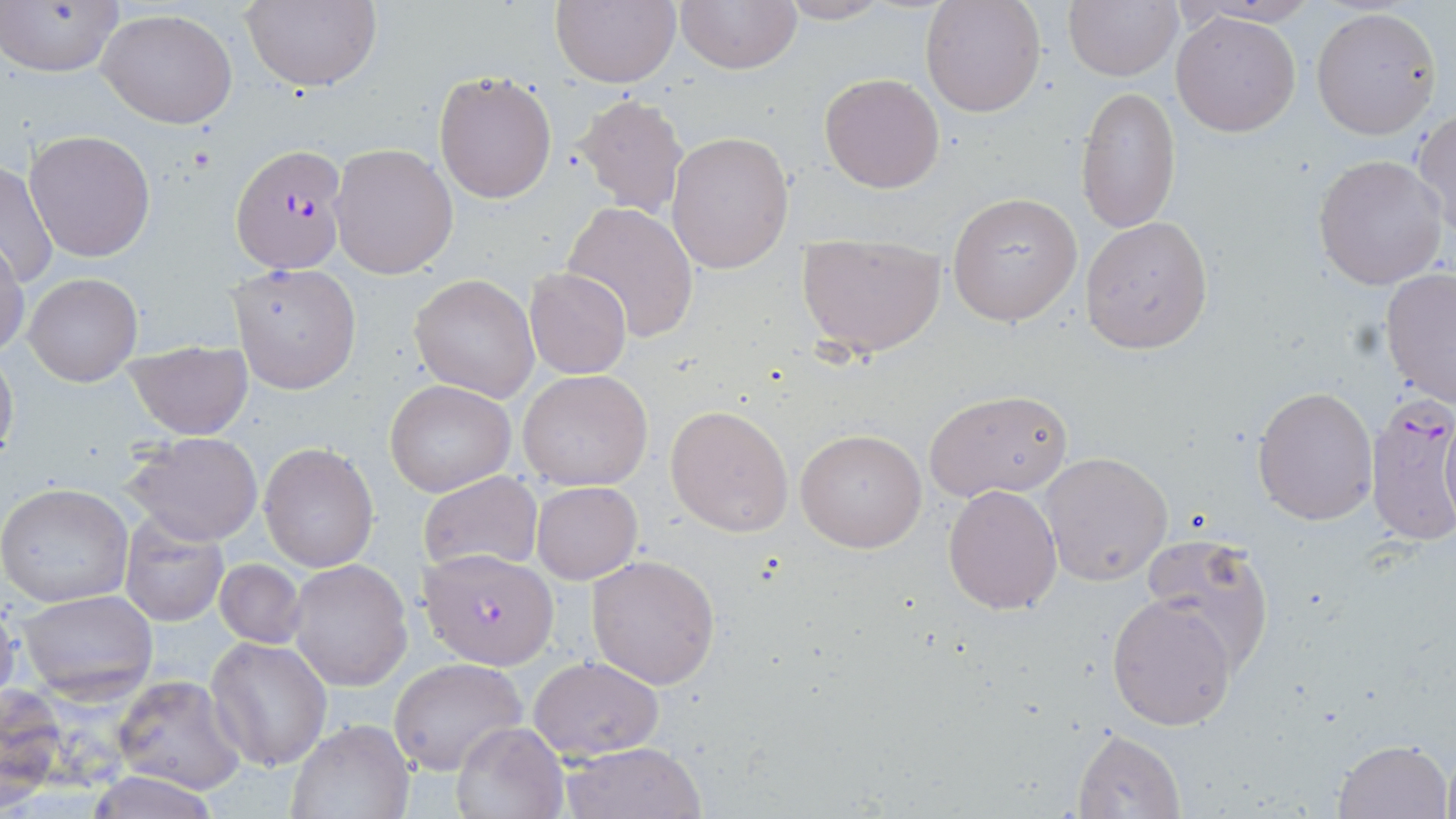

slide_level_diagnosis: Plasmodium falciparum
modality: optical microscopy
uninfected_red_blood_cell_locations: 'approximate bounding boxes as [x1, y1, x2, y2] in pixels: [549, 0, 680, 88], [674, 0, 802, 75], [769, 0, 896, 24], [920, 0, 1046, 118], [1063, 0, 1181, 81], [1180, 0, 1323, 28], [1, 1, 126, 79], [240, 1, 382, 91], [1312, 6, 1443, 141], [97, 7, 239, 128], [1171, 11, 1301, 137], [433, 70, 557, 204], [819, 74, 946, 192], [1075, 87, 1180, 234], [572, 92, 690, 219], [1412, 110, 1455, 235], [25, 129, 155, 261], [666, 130, 794, 273], [330, 143, 458, 279], [1312, 153, 1450, 291], [1, 160, 58, 290], [947, 191, 1082, 327], [560, 201, 699, 342], [1082, 216, 1213, 353], [796, 232, 947, 359], [0, 238, 26, 359], [229, 261, 362, 395], [524, 267, 633, 379], [1379, 269, 1456, 410], [24, 272, 141, 386], [411, 274, 539, 400], [125, 339, 254, 440], [0, 348, 19, 466], [518, 369, 653, 491], [385, 381, 514, 497], [1252, 385, 1378, 524], [923, 389, 1074, 501], [666, 404, 793, 539], [796, 428, 928, 554], [123, 431, 264, 547], [260, 442, 378, 572], [1039, 452, 1173, 586], [418, 470, 543, 578], [532, 481, 642, 584], [942, 482, 1063, 615], [0, 483, 133, 607], [118, 514, 229, 628], [1140, 533, 1275, 673], [586, 554, 721, 689], [213, 559, 306, 649], [287, 560, 413, 692], [16, 590, 159, 702], [1106, 592, 1238, 730], [0, 598, 22, 708], [207, 637, 330, 772], [530, 656, 664, 760], [390, 657, 527, 774], [111, 674, 245, 792], [1, 687, 63, 798], [286, 719, 413, 818], [448, 720, 567, 819], [1071, 727, 1186, 818], [1332, 736, 1451, 817], [557, 741, 707, 819], [1440, 751, 1456, 819], [86, 773, 219, 818]'
field_of_view: single
stain: May-Grünwald-Giemsa
image_size: 1456×819 pixels
preparation: thin blood film
plasmodium_falciparum_infected_red_blood_cell_locations: 'approximate bounding boxes as [x1, y1, x2, y2] in pixels: [231, 143, 348, 273], [1364, 397, 1456, 547], [423, 550, 557, 670]'
magnification: 1000x